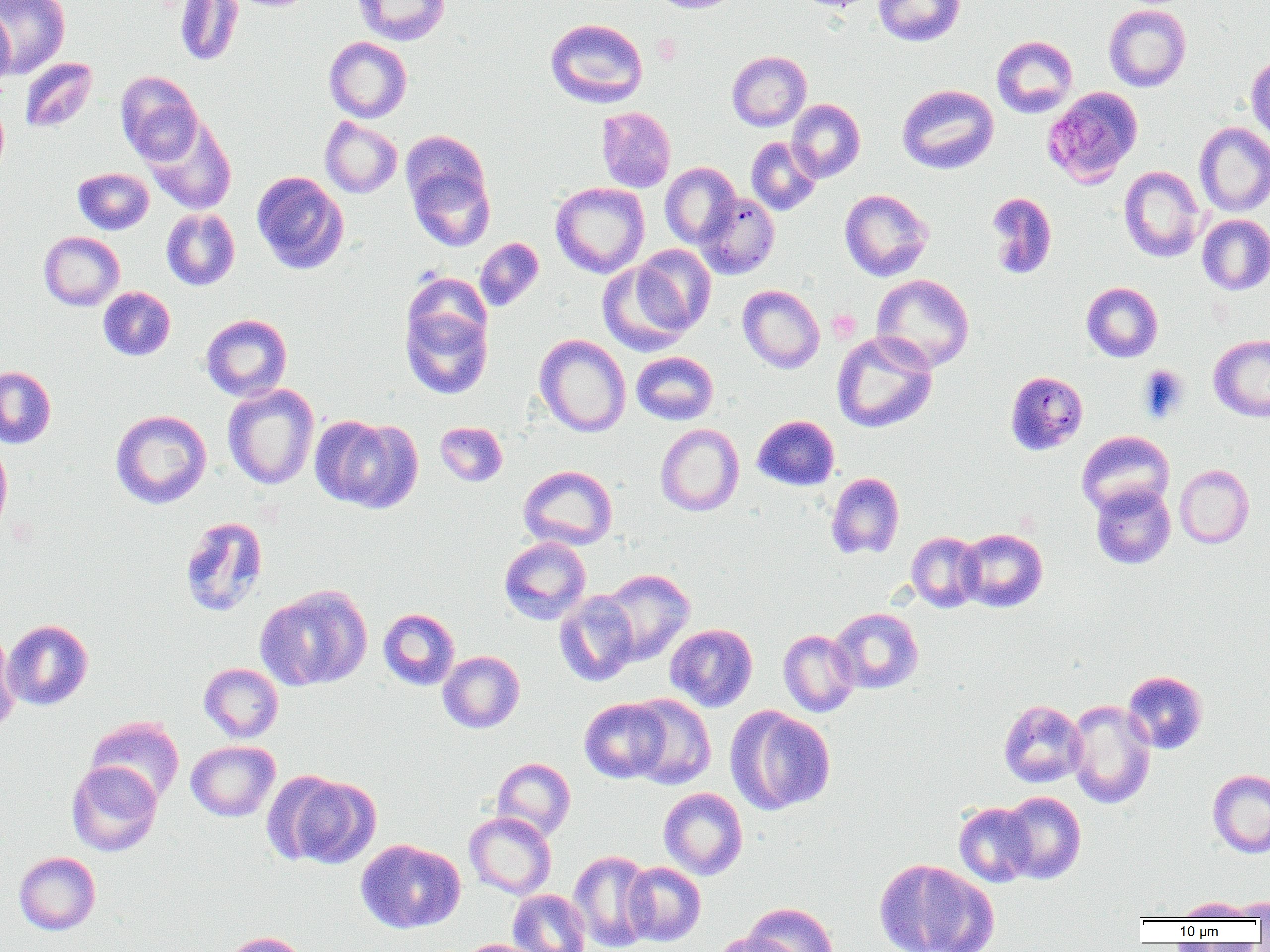
Approximate bounding boxes as (x1,y1)-(x2,y2) corner pairs in pixels. Platelet locations: (652,33)-(682,65), (828,310)-(861,343). Uninfected red blood cell locations: (1,0)-(70,77), (173,0)-(244,67), (352,0)-(450,45), (649,0)-(743,14), (873,0)-(965,46), (1103,4)-(1191,92), (0,9)-(15,94), (545,18)-(648,108), (991,35)-(1078,118), (324,36)-(412,122), (726,50)-(812,132), (1246,52)-(1270,146), (19,57)-(98,134), (115,71)-(204,166), (897,84)-(998,174), (0,99)-(9,182), (787,99)-(865,182), (596,106)-(675,193), (143,116)-(237,214), (320,117)-(402,198), (1194,123)-(1270,216), (745,137)-(821,216), (404,144)-(496,252), (660,162)-(741,248), (1118,165)-(1206,263), (73,167)-(154,234), (251,171)-(349,274), (550,182)-(650,278), (839,189)-(933,281), (985,192)-(1057,279), (695,193)-(780,279), (161,208)-(240,290), (1197,214)-(1270,295), (38,231)-(124,311), (474,238)-(544,311), (631,244)-(716,334), (597,262)-(692,355), (871,274)-(975,373), (1082,282)-(1163,362), (737,284)-(824,373), (98,286)-(175,361), (400,298)-(493,400), (201,314)-(292,401), (831,331)-(937,433), (534,334)-(631,437), (1209,335)-(1270,422), (631,352)-(719,425), (0,366)-(56,449), (1004,370)-(1088,455), (222,384)-(319,490), (110,410)-(212,509), (312,415)-(422,513), (752,415)-(840,491), (434,421)-(508,487), (655,424)-(744,516), (1077,431)-(1174,517), (0,437)-(13,539), (1175,464)-(1254,548), (518,465)-(617,550), (826,472)-(905,560), (1090,484)-(1176,569), (179,516)-(268,618), (957,528)-(1047,612), (906,532)-(984,612), (499,537)-(591,625), (599,568)-(694,665), (255,584)-(373,691), (554,591)-(639,686), (829,608)-(924,694), (378,609)-(460,690), (2,619)-(94,710), (665,623)-(758,711), (778,629)-(860,717), (0,631)-(19,736), (438,651)-(525,733), (199,663)-(284,742), (1122,671)-(1208,754), (625,694)-(716,789), (580,697)-(671,783), (998,699)-(1087,788), (1066,699)-(1156,809), (727,706)-(836,815), (85,716)-(184,806), (186,741)-(280,821), (492,757)-(575,841), (67,761)-(162,857), (1208,769)-(1270,858), (269,771)-(380,869), (658,787)-(748,879), (999,791)-(1086,883), (954,802)-(1037,886), (464,811)-(556,899), (355,839)-(465,934), (569,850)-(657,951), (14,851)-(101,935), (874,859)-(997,952), (623,862)-(706,946), (508,890)-(591,952), (1226,897)-(1270,920), (1176,898)-(1252,920), (743,902)-(839,952), (218,931)-(311,952), (710,932)-(796,952), (456,938)-(546,952). Plasmodium malariae-infected red blood cell locations: (1042,87)-(1143,188). Slide-level diagnosis: Plasmodium malariae. Image is 1270×952 pixels. Light microscopy. One field of a larger specimen. 1000x magnification. Thin blood smear.